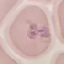
Summary:
  - Malaria status: parasitized
  - Stain: Giemsa
  - Image type: cell patch, automatically extracted from a larger field of view and resized to 64 × 64 pixels
  - Capture: smartphone through the microscope eyepiece
  - Preparation: thin blood film